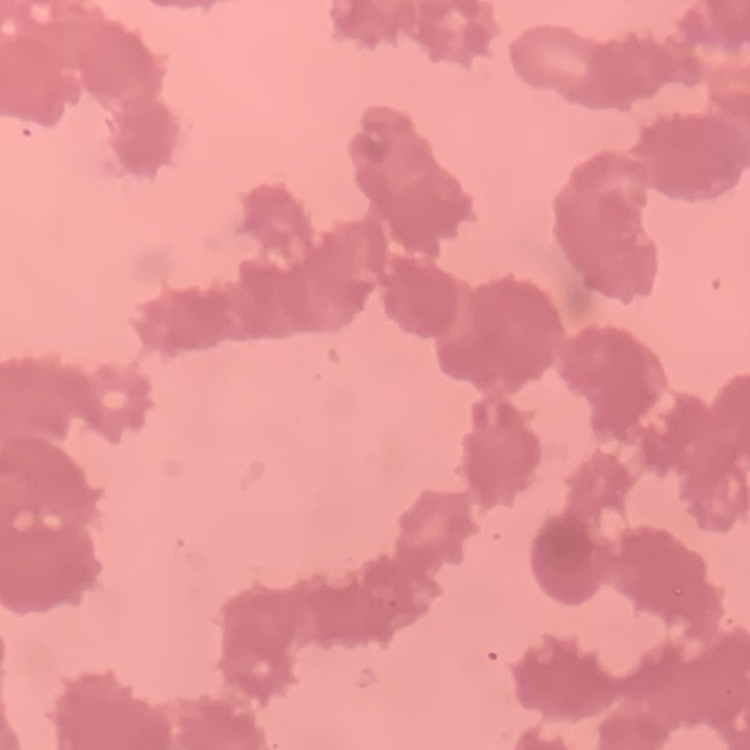

Summary:
  - Erythrocyte morphology: rouleaux formation
  - Preparation: thin blood film
  - Image type: one tile cut from a larger photomicrograph
  - Stain: Field's or Giemsa